Identify the parasite.
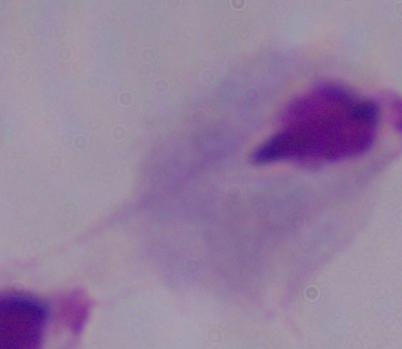
A trichomonad.

Summary:
  - Modality: photomicrograph
  - Magnification: 1000x